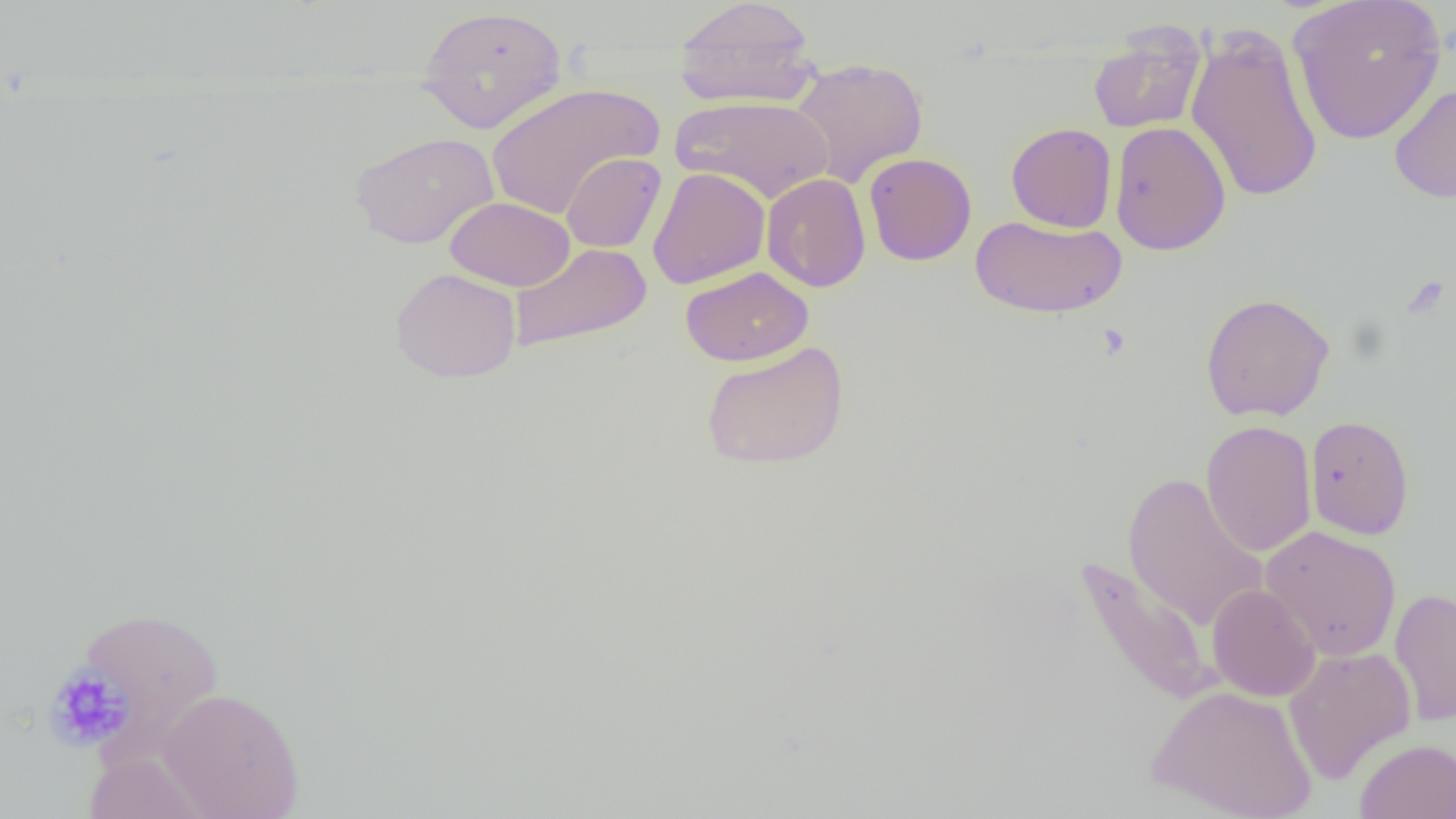
Summary:
  - Coordinate format: approximate bounding boxes as (x1, y1, x2, y2) in pixels
  - Uninfected red blood cell locations: (1287, 0, 1447, 146), (672, 1, 819, 108), (415, 4, 568, 133), (1088, 23, 1207, 134), (1185, 24, 1324, 204), (790, 57, 929, 188), (485, 82, 663, 220), (1389, 83, 1456, 204), (671, 95, 835, 204), (1109, 120, 1230, 256), (1006, 122, 1117, 233), (349, 131, 499, 250), (561, 152, 666, 253), (863, 153, 977, 266), (647, 167, 770, 289), (761, 173, 871, 292), (445, 196, 574, 291), (970, 215, 1126, 319), (508, 242, 652, 353), (680, 266, 813, 367), (390, 267, 521, 383), (1200, 292, 1335, 422), (700, 341, 850, 471), (1305, 414, 1414, 540), (1201, 421, 1317, 557), (1122, 472, 1268, 631), (1260, 525, 1401, 662), (1076, 557, 1219, 707), (1207, 583, 1320, 701), (1389, 587, 1456, 725), (76, 606, 225, 747), (1284, 646, 1416, 784), (1148, 685, 1317, 819), (157, 687, 305, 818), (1355, 740, 1456, 818), (83, 749, 217, 819)
  - Platelet locations: (1403, 277, 1451, 319), (1094, 322, 1133, 360), (42, 664, 137, 753)
  - Slide-level diagnosis: negative for blood parasites
  - Preparation: thin blood smear
  - Image size: 1456×819 pixels
  - Modality: light microscopy
  - Field of view: single
  - Magnification: 1000x